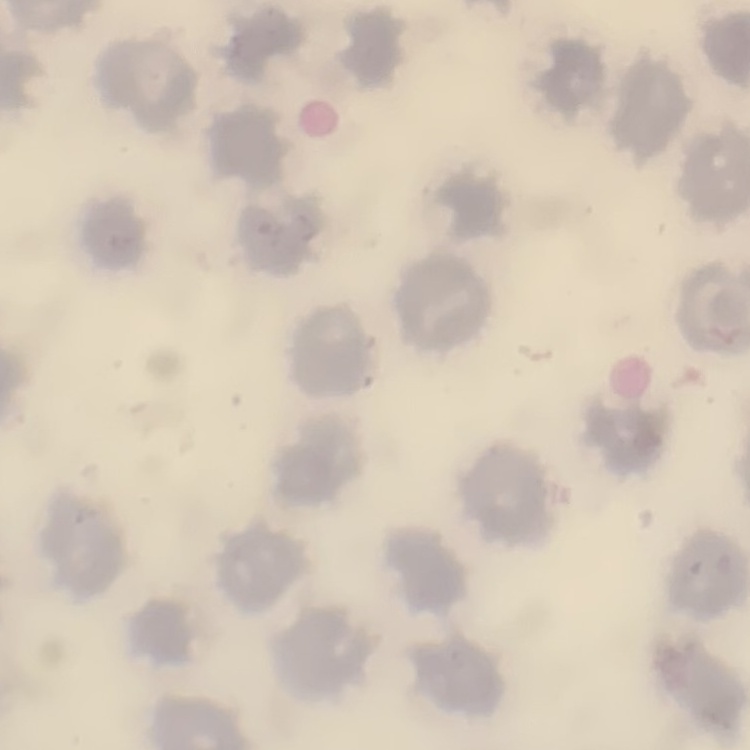

Summary:
  - Red blood cell morphology: no rouleaux formation
  - Image type: square crop of a larger photomicrograph
  - Preparation: thin blood film
  - Stain: Field's or Giemsa